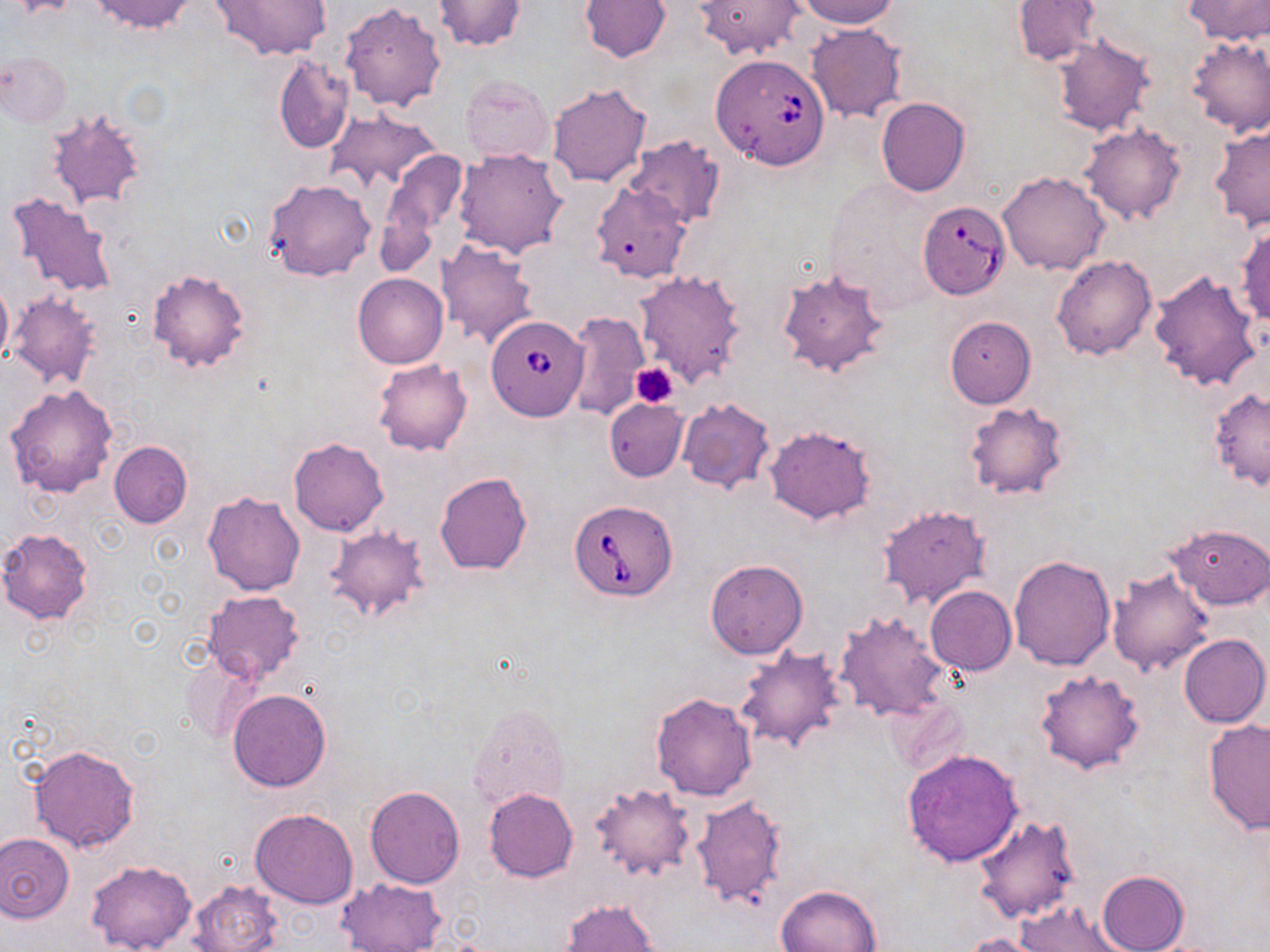
slide-level diagnosis = Babesia divergens
platelet locations = approximate bounding boxes as [x1, y1, x2, y2] in pixels: [632, 363, 680, 408]
image size = 1270×952 pixels
magnification = 1000x
modality = optical microscopy
stain = May-Grünwald-Giemsa
uninfected red blood cell locations = approximate bounding boxes as [x1, y1, x2, y2] in pixels: [90, 0, 198, 34], [212, 0, 332, 61], [433, 0, 526, 51], [798, 0, 900, 29], [1185, 0, 1269, 44], [579, 1, 670, 62], [695, 1, 804, 61], [1013, 1, 1100, 66], [339, 2, 445, 112], [805, 24, 907, 124], [1051, 35, 1154, 137], [1184, 35, 1270, 137], [1, 52, 72, 127], [273, 56, 354, 153], [460, 75, 553, 166], [545, 81, 652, 189], [876, 97, 970, 196], [45, 107, 148, 211], [326, 109, 441, 194], [1078, 122, 1186, 223], [1209, 127, 1269, 233], [623, 136, 726, 229], [453, 147, 569, 259], [377, 148, 470, 262], [998, 171, 1111, 277], [263, 178, 376, 282], [589, 181, 691, 283], [6, 191, 120, 300], [1235, 219, 1270, 328], [436, 239, 538, 349], [1053, 254, 1157, 359], [776, 267, 892, 380], [146, 268, 252, 373], [634, 269, 747, 387], [1148, 269, 1263, 393], [353, 273, 447, 370], [0, 279, 13, 367], [8, 291, 103, 390], [566, 311, 648, 420], [944, 316, 1036, 407], [372, 359, 473, 456], [4, 383, 118, 498], [1207, 387, 1270, 490], [604, 399, 688, 481], [676, 399, 775, 494], [963, 401, 1070, 501], [765, 424, 876, 523], [288, 437, 389, 537], [108, 441, 192, 528], [434, 472, 532, 575], [202, 490, 306, 596], [876, 504, 991, 609], [1167, 524, 1270, 609], [324, 525, 430, 626], [0, 527, 93, 624], [1008, 554, 1116, 670], [705, 558, 808, 659], [1106, 567, 1214, 675], [925, 586, 1017, 675], [202, 590, 304, 685], [834, 611, 948, 722], [1179, 633, 1269, 728], [738, 649, 847, 754], [1032, 667, 1145, 775], [227, 688, 332, 792], [650, 692, 757, 801], [886, 696, 971, 777], [468, 702, 570, 811], [1202, 719, 1270, 834], [27, 743, 141, 853], [901, 747, 1024, 866], [590, 781, 695, 881], [365, 785, 465, 888], [484, 788, 578, 883], [690, 793, 787, 910], [250, 808, 358, 908], [973, 813, 1082, 925], [0, 832, 75, 922], [86, 859, 197, 952], [1097, 871, 1189, 952], [337, 876, 446, 951], [187, 878, 283, 952], [775, 883, 884, 952], [561, 899, 659, 952], [1016, 899, 1126, 952], [960, 933, 1046, 952]
preparation = thin blood smear
field of view = one of a larger specimen
Babesia divergens-infected red blood cell locations = approximate bounding boxes as [x1, y1, x2, y2] in pixels: [710, 54, 830, 169], [918, 202, 1009, 298], [487, 316, 590, 422], [568, 499, 678, 602]